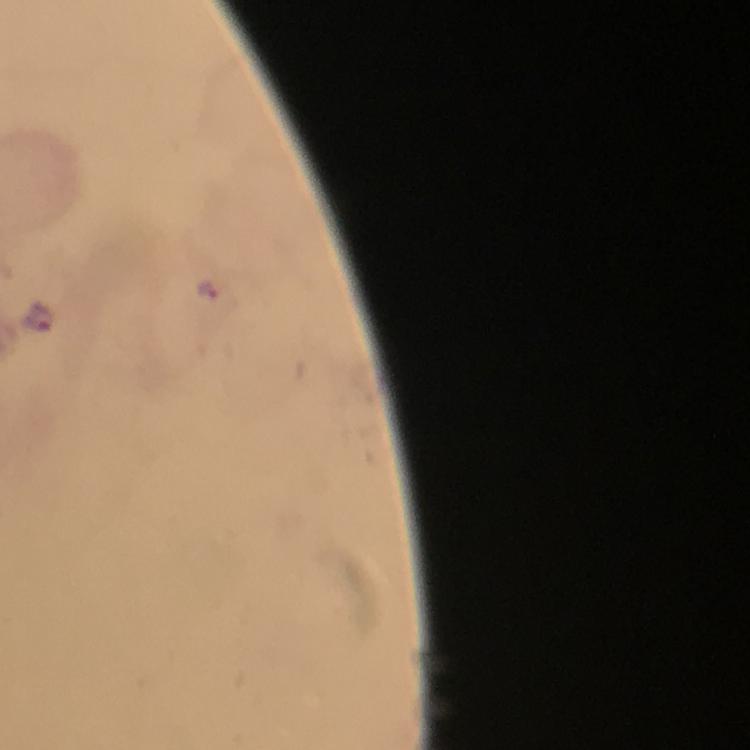

malaria_parasite_locations: 'approximate object centers, in pixels from the top-left corner: (x=207, y=292), (x=39, y=318)'
magnification: 100x
stain: Giemsa
image_size: 750×750 pixels
immersion_oil: applied
preparation: thick smear
context: from a malaria diagnostic workup
capture: smartphone mounted on the microscope
cropped_from: one field of view